Report the malaria status of this cell.
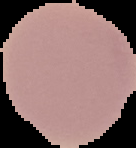
It is uninfected.

Summary:
  - Image size: 136×148 pixels
  - Image type: segmented cell region on a black background
  - Preparation: thin blood film